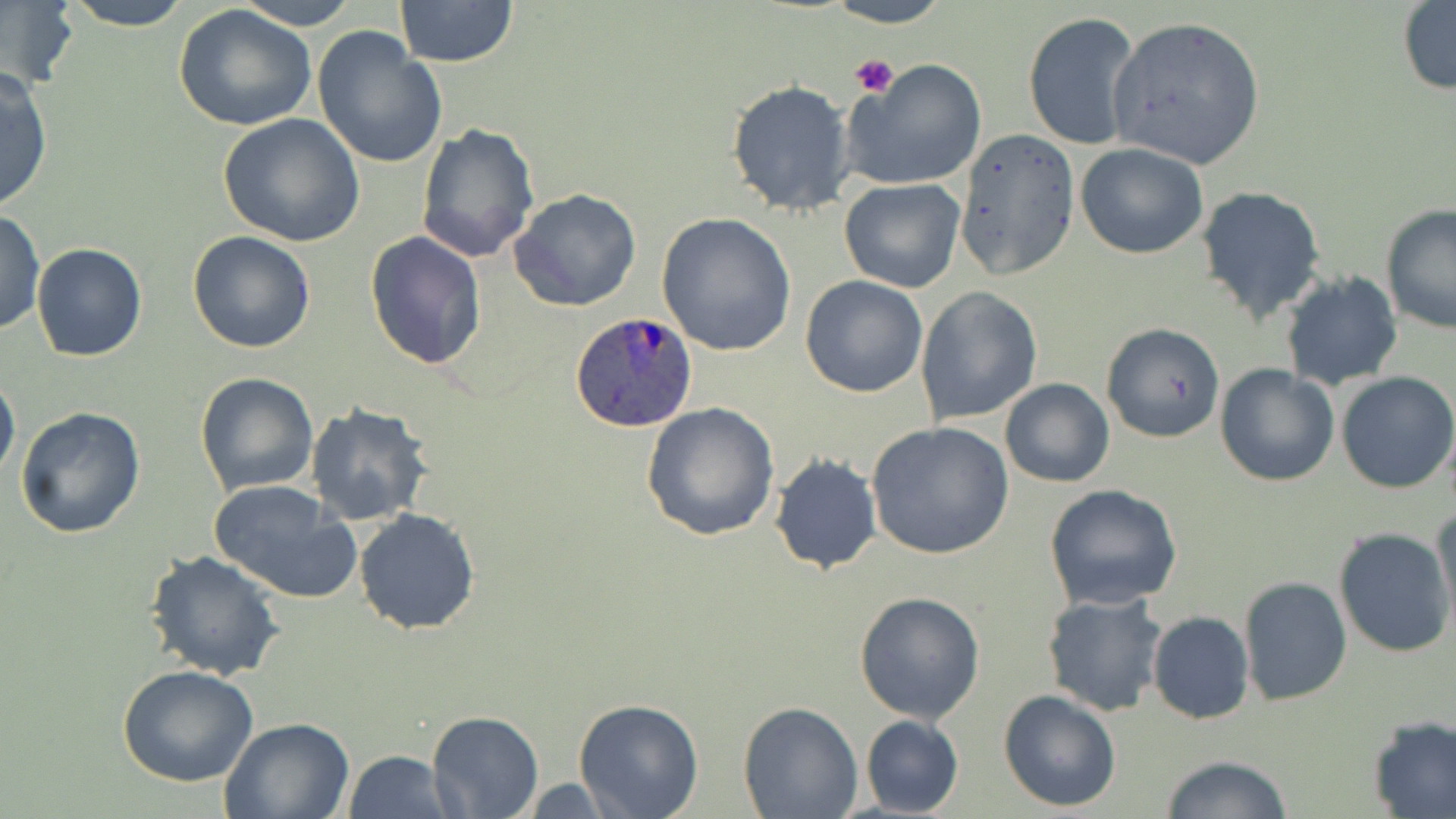

Approximate bounding boxes as named x1/y1/x2/y2 corners in pixels. Uninfected red blood cell locations: (x1=62, y1=0, x2=194, y2=31), (x1=232, y1=0, x2=361, y2=30), (x1=393, y1=0, x2=519, y2=67), (x1=824, y1=0, x2=951, y2=28), (x1=1397, y1=1, x2=1456, y2=96), (x1=2, y1=2, x2=77, y2=91), (x1=173, y1=5, x2=317, y2=133), (x1=1023, y1=11, x2=1144, y2=154), (x1=1107, y1=15, x2=1266, y2=170), (x1=312, y1=27, x2=448, y2=171), (x1=847, y1=58, x2=990, y2=188), (x1=0, y1=66, x2=54, y2=213), (x1=726, y1=79, x2=856, y2=215), (x1=219, y1=113, x2=367, y2=248), (x1=416, y1=123, x2=540, y2=265), (x1=953, y1=127, x2=1078, y2=279), (x1=1075, y1=142, x2=1208, y2=259), (x1=840, y1=178, x2=966, y2=293), (x1=1197, y1=185, x2=1328, y2=326), (x1=509, y1=189, x2=643, y2=312), (x1=1379, y1=203, x2=1455, y2=334), (x1=1, y1=209, x2=45, y2=334), (x1=656, y1=211, x2=798, y2=357), (x1=365, y1=230, x2=487, y2=371), (x1=186, y1=231, x2=316, y2=354), (x1=32, y1=243, x2=147, y2=361), (x1=1278, y1=270, x2=1403, y2=391), (x1=800, y1=274, x2=928, y2=397), (x1=914, y1=286, x2=1043, y2=425), (x1=1101, y1=321, x2=1225, y2=444), (x1=1215, y1=364, x2=1340, y2=487), (x1=0, y1=368, x2=20, y2=485), (x1=194, y1=371, x2=320, y2=496), (x1=1336, y1=372, x2=1456, y2=493), (x1=999, y1=378, x2=1115, y2=487), (x1=641, y1=402, x2=782, y2=541), (x1=303, y1=403, x2=436, y2=529), (x1=16, y1=407, x2=146, y2=540), (x1=866, y1=420, x2=1014, y2=561), (x1=769, y1=451, x2=882, y2=575), (x1=209, y1=479, x2=362, y2=605), (x1=1043, y1=484, x2=1185, y2=610), (x1=1433, y1=504, x2=1456, y2=630), (x1=354, y1=507, x2=481, y2=635), (x1=1332, y1=527, x2=1455, y2=659), (x1=145, y1=550, x2=286, y2=682), (x1=1238, y1=577, x2=1352, y2=707), (x1=853, y1=591, x2=986, y2=723), (x1=1042, y1=592, x2=1168, y2=716), (x1=1147, y1=611, x2=1254, y2=724), (x1=117, y1=665, x2=260, y2=787), (x1=998, y1=689, x2=1123, y2=812), (x1=573, y1=698, x2=704, y2=819), (x1=737, y1=700, x2=864, y2=818), (x1=428, y1=708, x2=543, y2=817), (x1=860, y1=715, x2=964, y2=817), (x1=1367, y1=715, x2=1456, y2=818), (x1=219, y1=717, x2=353, y2=819), (x1=343, y1=751, x2=454, y2=819), (x1=1159, y1=755, x2=1295, y2=818), (x1=507, y1=777, x2=628, y2=815). Plasmodium ovale-infected red blood cell locations: (x1=570, y1=311, x2=701, y2=433). Platelet locations: (x1=851, y1=54, x2=900, y2=98). Slide-level diagnosis: Plasmodium ovale. 1000x magnification. Single field of view. Image is 1456×819 pixels. May-Grünwald-Giemsa stain. Optical microscopy. Thin blood smear.